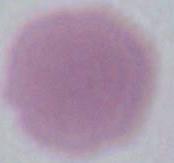

identification = red blood cell
modality = micrograph
magnification = 1000x